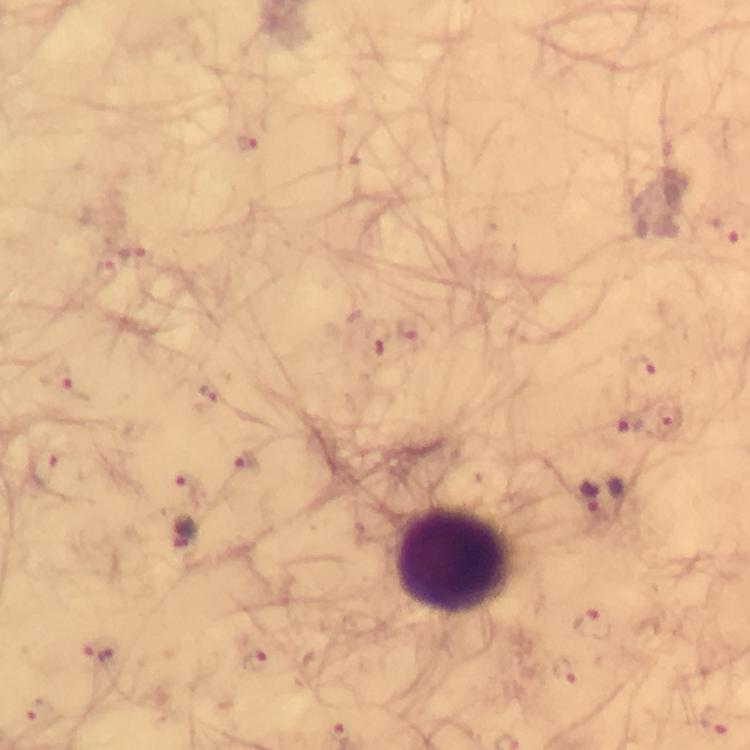

context = from a diagnostic examination for malaria
immersion oil = used
stain = Giemsa
image size = 750×750 pixels
leukocyte locations = approximate centers as {x, y} in pixels: {453, 558}
preparation = thick smear
malaria parasite locations = approximate centers as {x, y} in pixels: {248, 145}, {727, 234}, {132, 254}, {411, 328}, {377, 350}, {643, 368}, {63, 380}, {211, 393}, {630, 424}, {669, 424}, {247, 464}, {45, 467}, {186, 485}, {591, 498}, {593, 623}, {102, 655}, {252, 658}, {563, 673}, {38, 713}, {715, 722}
cropped from = one field of view
capture = smartphone camera through the microscope
magnification = 100x